State which parasite is depicted.
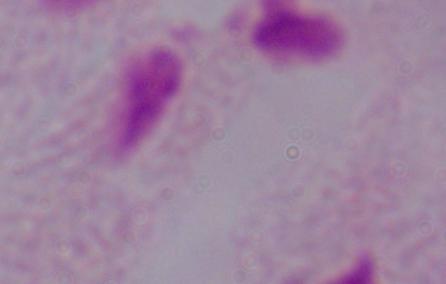

A trichomonad.

Photomicrograph. 1000x magnification.